Locate every Plasmodium parasite and every leukocyte.
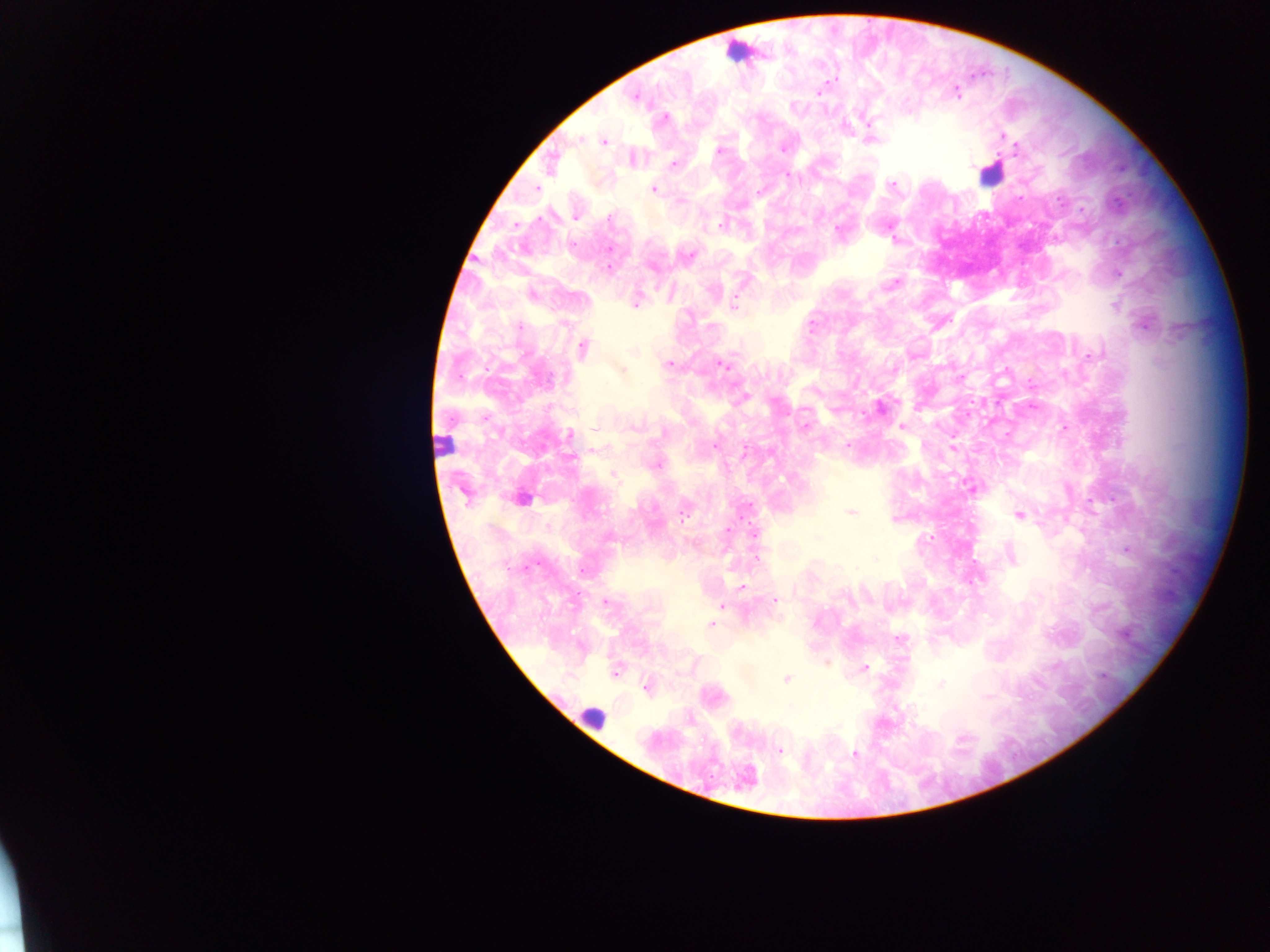
Approximate centers as {x, y} in pixels.
Plasmodium parasites: {819, 92}, {956, 93}, {635, 98}, {664, 118}, {868, 122}, {1002, 136}, {580, 140}, {603, 142}, {782, 149}, {1016, 149}, {719, 150}, {674, 163}, {971, 166}, {790, 175}, {892, 184}, {537, 188}, {653, 189}, {759, 192}, {576, 217}, {610, 217}, {721, 224}, {838, 229}, {894, 239}, {690, 255}, {608, 268}, {894, 283}, {532, 294}, {635, 303}, {735, 303}, {1115, 305}, {811, 325}, {1144, 325}, {519, 326}, {583, 348}, {1091, 355}, {669, 364}, {723, 365}, {621, 370}, {743, 398}, {879, 407}, {805, 426}, {901, 426}, {634, 427}, {662, 432}, {1007, 433}, {570, 435}, {715, 445}, {847, 445}, {952, 448}, {596, 449}, {744, 451}, {656, 465}, {612, 475}, {970, 486}, {523, 499}, {852, 512}, {684, 514}, {1019, 514}, {549, 526}, {728, 530}, {931, 536}, {1127, 549}, {756, 558}, {855, 568}, {742, 587}, {776, 600}, {606, 602}, {721, 606}, {711, 624}, {900, 639}, {866, 667}, {614, 673}, {787, 678}, {940, 683}, {645, 687}, {779, 750}, {855, 754}.
Leukocytes: {740, 52}, {990, 177}, {443, 446}, {593, 717}.

country = Ghana
field of view = single
preparation = thick blood film
image size = 1270×952 pixels
capture = mobile-phone photograph through a microscope